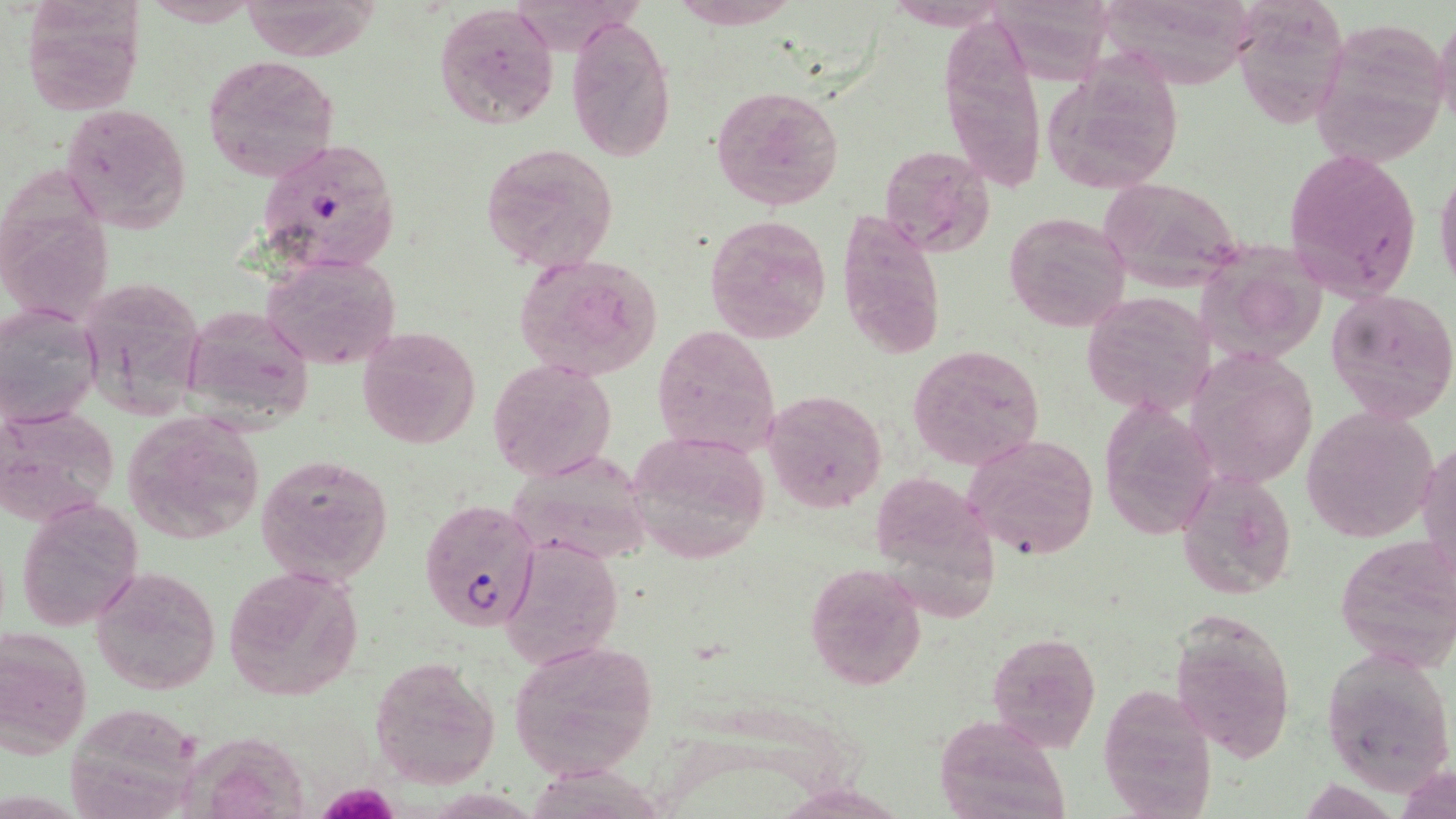

slide_level_diagnosis: Plasmodium falciparum
image_size: 1456×819 pixels
preparation: thin blood smear
magnification: 1000x
stain: May-Grünwald-Giemsa
plasmodium_falciparum_infected_red_blood_cell_locations: 'approximate bounding boxes as named x1/y1/x2/y2 corners in pixels: (x1=256, y1=138, x2=403, y2=279), (x1=419, y1=498, x2=541, y2=631)'
modality: light microscopy
field_of_view: single
uninfected_red_blood_cell_locations: 'approximate bounding boxes as named x1/y1/x2/y2 corners in pixels: (x1=17, y1=0, x2=147, y2=115), (x1=141, y1=0, x2=262, y2=28), (x1=671, y1=0, x2=800, y2=29), (x1=1240, y1=0, x2=1357, y2=131), (x1=1100, y1=1, x2=1268, y2=93), (x1=433, y1=3, x2=560, y2=128), (x1=998, y1=3, x2=1126, y2=93), (x1=1432, y1=10, x2=1456, y2=137), (x1=937, y1=16, x2=1048, y2=195), (x1=567, y1=17, x2=676, y2=162), (x1=1309, y1=18, x2=1450, y2=167), (x1=203, y1=56, x2=340, y2=181), (x1=1038, y1=59, x2=1188, y2=198), (x1=711, y1=84, x2=843, y2=209), (x1=62, y1=103, x2=191, y2=233), (x1=483, y1=142, x2=619, y2=272), (x1=878, y1=145, x2=995, y2=257), (x1=1283, y1=145, x2=1422, y2=301), (x1=1434, y1=161, x2=1456, y2=296), (x1=1098, y1=177, x2=1245, y2=291), (x1=836, y1=206, x2=947, y2=360), (x1=1003, y1=212, x2=1132, y2=331), (x1=705, y1=214, x2=834, y2=344), (x1=1201, y1=239, x2=1328, y2=369), (x1=260, y1=249, x2=403, y2=373), (x1=514, y1=250, x2=666, y2=381), (x1=74, y1=276, x2=204, y2=417), (x1=1326, y1=287, x2=1456, y2=425), (x1=1081, y1=291, x2=1214, y2=417), (x1=1, y1=301, x2=104, y2=430), (x1=179, y1=302, x2=314, y2=428), (x1=357, y1=324, x2=482, y2=450), (x1=650, y1=325, x2=779, y2=458), (x1=907, y1=344, x2=1045, y2=469), (x1=1183, y1=349, x2=1321, y2=490), (x1=487, y1=359, x2=616, y2=481), (x1=762, y1=389, x2=887, y2=512), (x1=1095, y1=400, x2=1219, y2=540), (x1=1302, y1=404, x2=1439, y2=542), (x1=1, y1=406, x2=117, y2=524), (x1=122, y1=411, x2=265, y2=544), (x1=628, y1=430, x2=772, y2=564), (x1=964, y1=434, x2=1097, y2=558), (x1=1418, y1=435, x2=1455, y2=590), (x1=255, y1=452, x2=395, y2=588), (x1=507, y1=452, x2=654, y2=566), (x1=1176, y1=470, x2=1298, y2=599), (x1=16, y1=498, x2=143, y2=632), (x1=1335, y1=532, x2=1454, y2=673), (x1=500, y1=533, x2=623, y2=670), (x1=805, y1=563, x2=925, y2=690), (x1=90, y1=564, x2=221, y2=696), (x1=225, y1=565, x2=365, y2=701), (x1=1166, y1=609, x2=1298, y2=764), (x1=1, y1=629, x2=92, y2=756), (x1=986, y1=632, x2=1100, y2=751), (x1=507, y1=638, x2=661, y2=781), (x1=1322, y1=646, x2=1455, y2=794), (x1=369, y1=656, x2=500, y2=790), (x1=1096, y1=686, x2=1214, y2=818), (x1=69, y1=705, x2=200, y2=816), (x1=935, y1=713, x2=1071, y2=819), (x1=170, y1=734, x2=316, y2=819)'